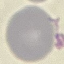

Malaria status: uninfected. Giemsa-stained preparation. Automatically extracted cell patch, resized to 64 × 64 pixels. Thin blood film. Photographed with a smartphone camera at the microscope eyepiece.